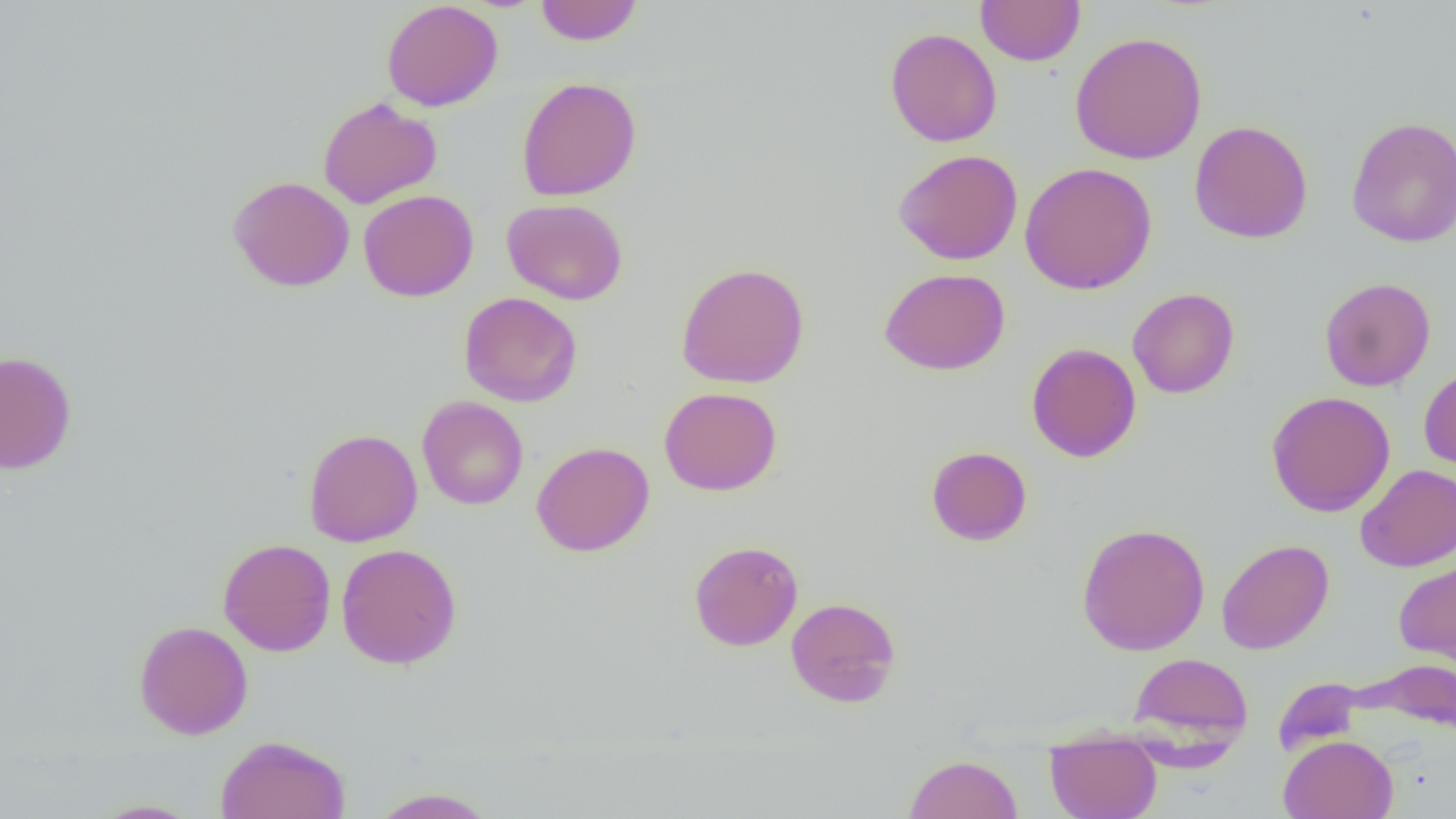
slide_level_diagnosis: no evidence of blood parasites
modality: optical microscopy
uninfected_red_blood_cell_locations: 'approximate bounding boxes as (x1,y1)-(x2,y2) corner pairs in pixels: (975,0)-(1086,66), (381,1)-(504,111), (535,1)-(643,45), (884,27)-(1002,147), (1069,31)-(1207,165), (516,77)-(642,201), (318,97)-(442,208), (1345,116)-(1456,247), (1189,120)-(1313,244), (893,149)-(1023,265), (1019,162)-(1157,295), (227,175)-(355,292), (358,190)-(479,302), (501,198)-(628,305), (676,262)-(810,388), (879,268)-(1010,376), (1319,277)-(1436,391), (1127,287)-(1240,399), (459,291)-(583,407), (1026,342)-(1141,462), (0,350)-(77,475), (1419,365)-(1456,474), (659,386)-(783,496), (1266,391)-(1396,517), (416,396)-(529,510), (303,428)-(422,547), (531,442)-(655,557), (926,446)-(1032,546), (1355,464)-(1456,572), (1076,522)-(1211,656), (218,538)-(336,656), (1216,539)-(1334,655), (688,540)-(803,651), (336,543)-(462,669), (1393,557)-(1456,670), (785,597)-(902,707), (134,621)-(253,739), (1128,651)-(1254,750), (1360,659)-(1456,734), (1045,732)-(1161,819), (215,734)-(352,819), (1279,734)-(1398,819), (903,753)-(1023,819), (367,787)-(499,818), (88,799)-(204,818)'
field_of_view: one of a larger specimen
preparation: thin blood smear
magnification: 1000x
image_size: 1456×819 pixels